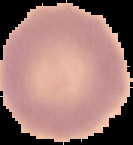
{
  "preparation": "thin blood film",
  "image_type": "segmented cell region with the area outside set to black",
  "malaria_status": "uninfected",
  "image_size": "133×145 pixels"
}